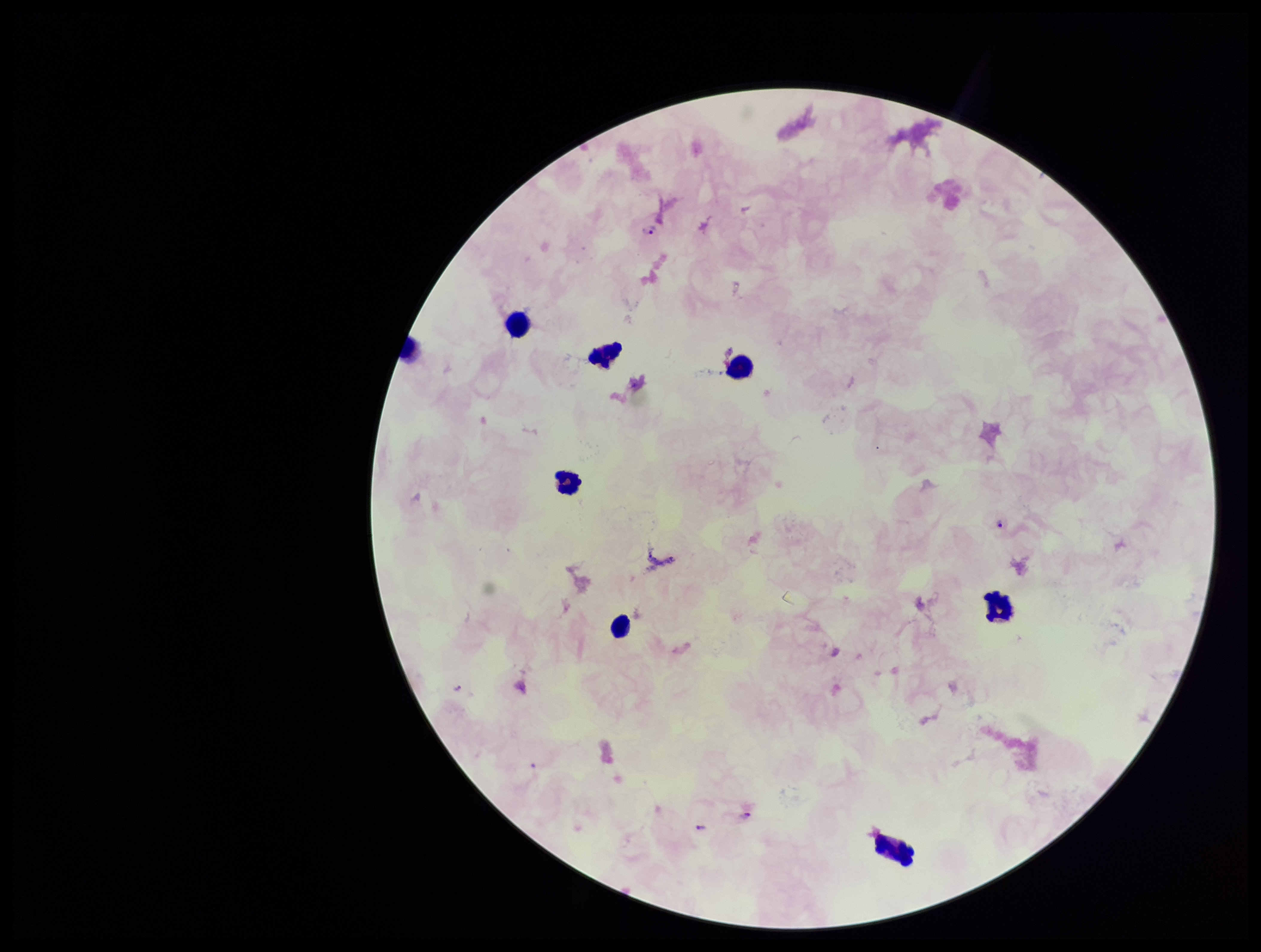 Plasmodium parasites: seen. Preparation: thick smear. Photographed through the microscope eyepiece with a smartphone camera. Single field of view. Parasite count: 5. Species reported for this patient: Plasmodium falciparum. Image is 1261×952 pixels. Stained with Giemsa. Patient malaria status: infected. Leukocyte count: 7.